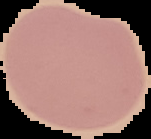
Summary:
  - Image type: segmented cell region on a black background
  - Image size: 151×139 pixels
  - Preparation: thin blood film
  - Malaria status: uninfected